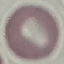

result = negative for malaria parasites
image type = cell patch, automatically extracted from a larger field of view and resized to 64 × 64 pixels
stain = Giemsa
capture = smartphone through the microscope eyepiece
preparation = thin blood film